Point out each Plasmodium parasite.
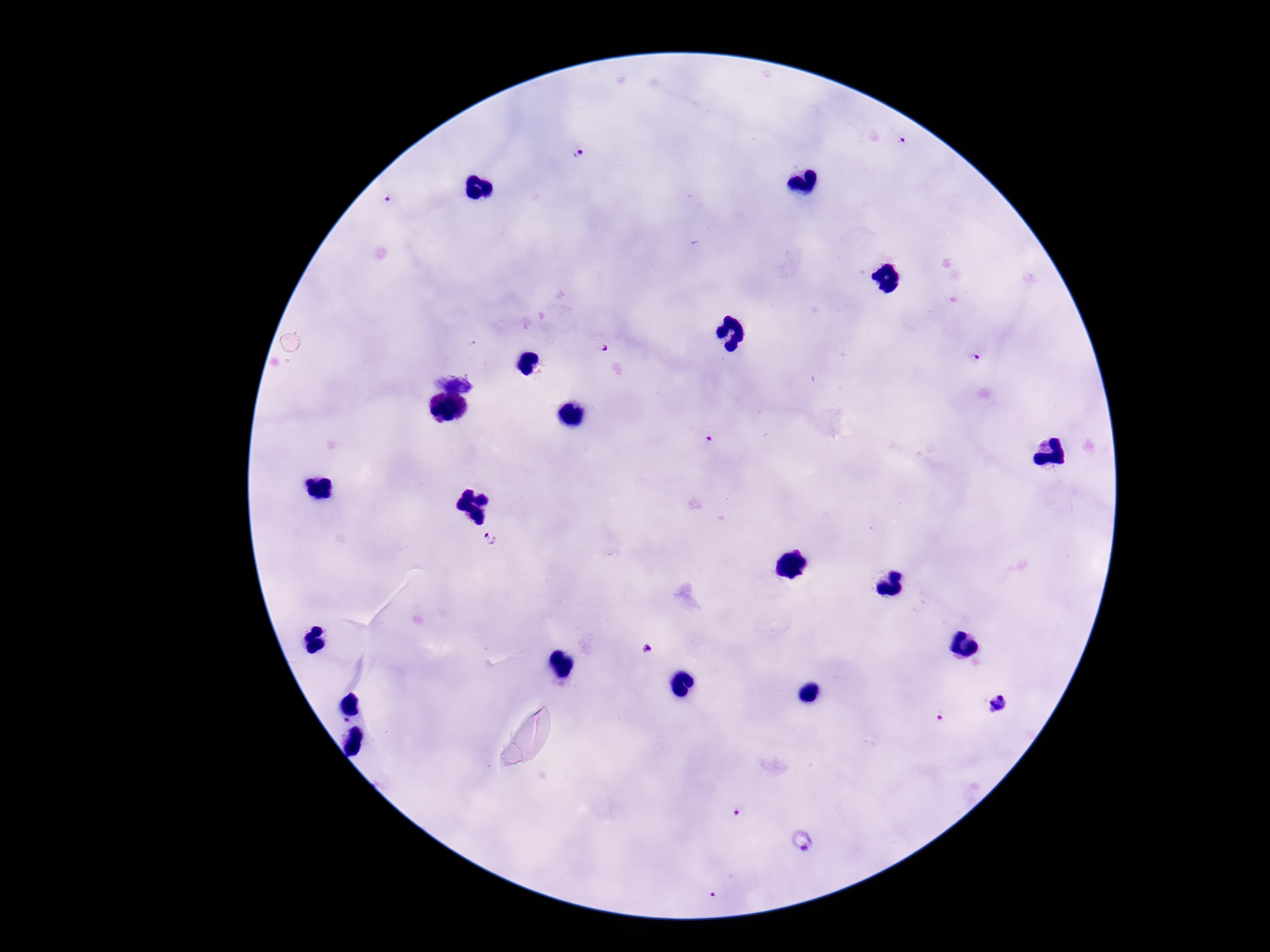

Approximate centers as (x, y) in pixels.
Plasmodium parasites: (905, 142), (579, 150), (387, 200), (602, 347), (976, 360), (708, 440), (491, 538), (647, 649), (1000, 705), (737, 813).

Summary:
  - Image size: 1270×952 pixels
  - Preparation: thick peripheral-blood smear
  - Patient malaria status: infected
  - Stain: Giemsa
  - Field of view: one from this slide
  - Magnification: 100x
  - Capture: smartphone camera through the microscope eyepiece